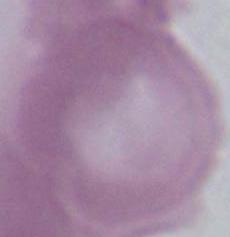

magnification: 1000x
modality: micrograph
identification: red blood cell